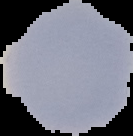
preparation: thin blood smear
image_type: segmented cell region on a black background
image_size: 133×136 pixels
malaria_status: uninfected